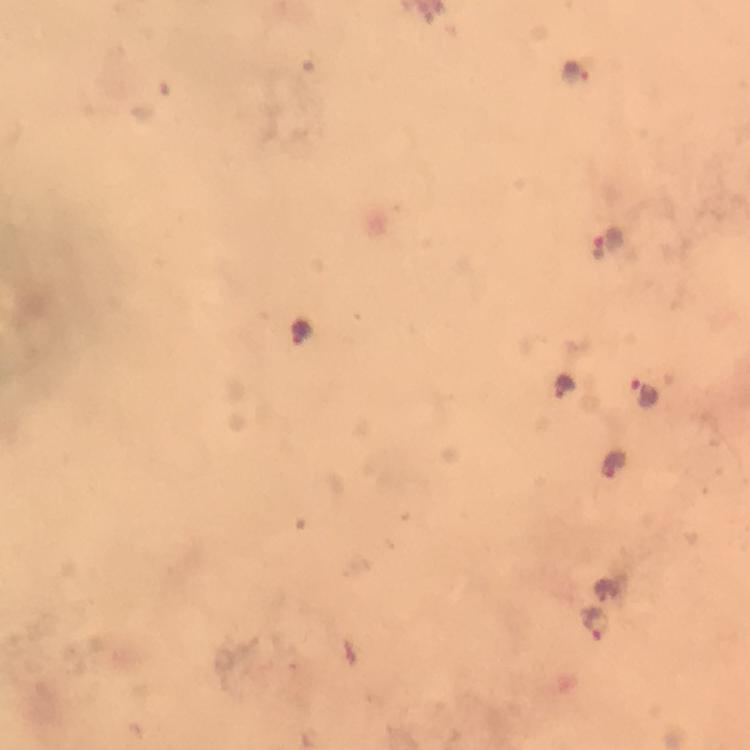

Approximate object centers, in pixels from the top-left corner.
Summary:
  - Malaria parasite locations: (x=576, y=69), (x=600, y=248), (x=565, y=386), (x=643, y=392), (x=612, y=466), (x=607, y=589), (x=594, y=624)
  - Capture: smartphone photograph through a microscope
  - Immersion oil: applied
  - Image size: 750×750 pixels
  - Stain: Giemsa
  - Cropped from: one field of view
  - Preparation: thick smear
  - Context: from a malaria diagnostic workup
  - Magnification: 100x